Give the position of every malaria parasite.
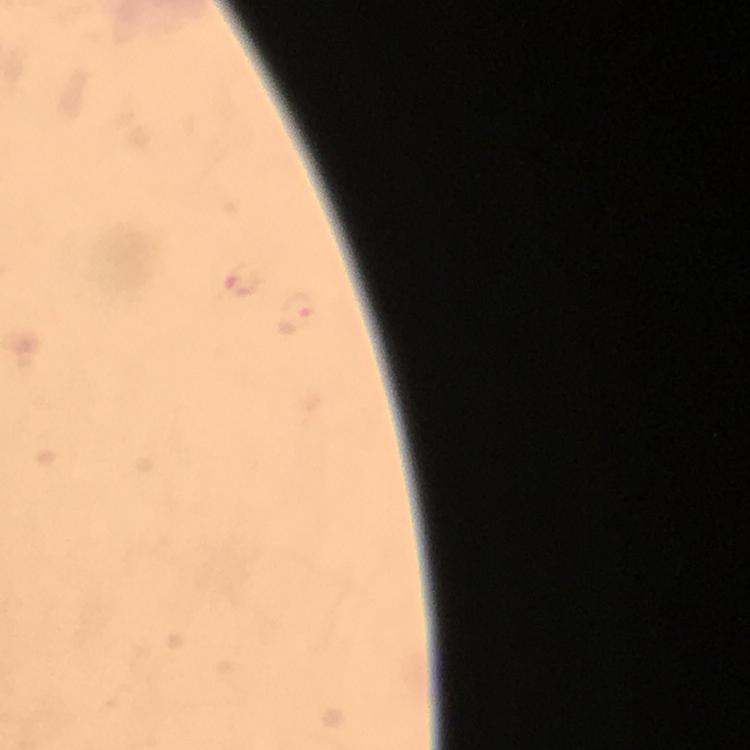
Approximate centers as {x, y} in pixels.
Malaria parasites: {240, 278}, {297, 314}.

Summary:
  - Image size: 750×750 pixels
  - Stain: Giemsa
  - Preparation: thick smear
  - Cropped from: a single field of view
  - Context: from a diagnostic examination for malaria
  - Immersion oil: applied
  - Magnification: 100x
  - Capture: smartphone photograph through a microscope